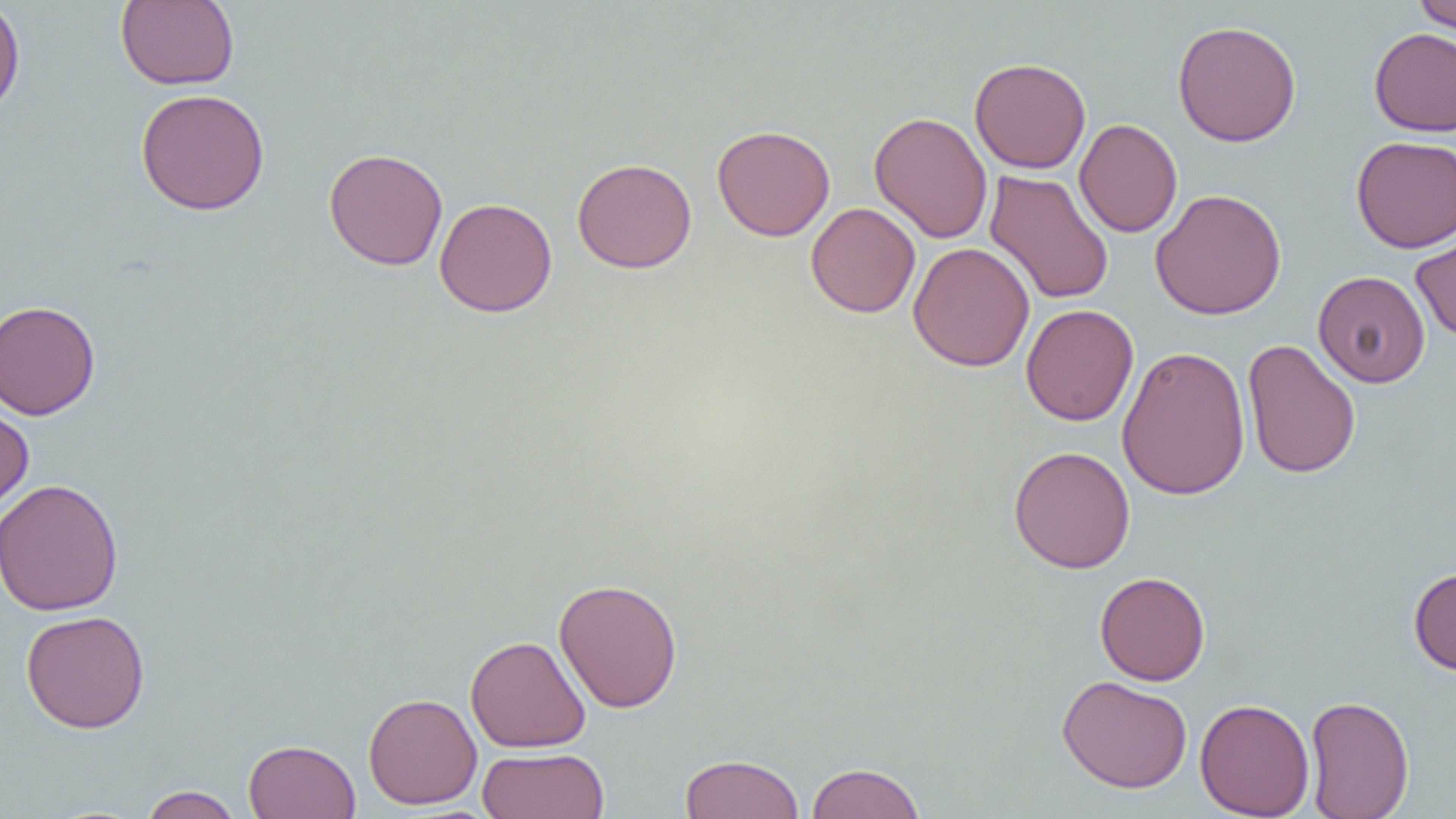

Summary:
  - Coordinate format: approximate bounding boxes as [x1, y1, x2, y2] in pixels
  - Uninfected red blood cell locations: [0, 0, 26, 120], [1412, 0, 1456, 36], [115, 1, 239, 90], [1172, 19, 1302, 146], [1368, 27, 1456, 137], [969, 57, 1092, 173], [135, 88, 270, 215], [869, 111, 993, 243], [1074, 118, 1183, 238], [712, 124, 835, 241], [1351, 135, 1456, 252], [323, 148, 449, 271], [572, 157, 697, 273], [984, 169, 1114, 306], [1150, 188, 1287, 320], [434, 197, 558, 317], [806, 202, 921, 319], [1410, 219, 1456, 342], [908, 242, 1035, 372], [1313, 270, 1430, 388], [0, 300, 101, 421], [1021, 304, 1138, 426], [1242, 339, 1361, 479], [1116, 345, 1251, 501], [0, 402, 34, 513], [1008, 445, 1136, 574], [0, 479, 125, 616], [1408, 567, 1456, 675], [1094, 571, 1210, 685], [553, 578, 683, 713], [20, 610, 150, 733], [465, 635, 591, 753], [1057, 674, 1192, 793], [363, 692, 482, 809], [1303, 695, 1414, 819], [1195, 697, 1315, 818], [243, 739, 361, 819], [477, 747, 609, 819], [680, 753, 804, 819], [805, 761, 926, 819], [139, 785, 244, 819]
  - Slide-level diagnosis: no evidence of blood parasites
  - Magnification: 1000x
  - Image size: 1456×819 pixels
  - Modality: light microscopy
  - Preparation: thin blood smear
  - Field of view: single